Assess this cell for malaria.
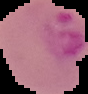
Parasitized.

Summary:
  - Image type: segmented cell region on a black background
  - Image size: 88×94 pixels
  - Preparation: thin blood smear